Classify the preparation.
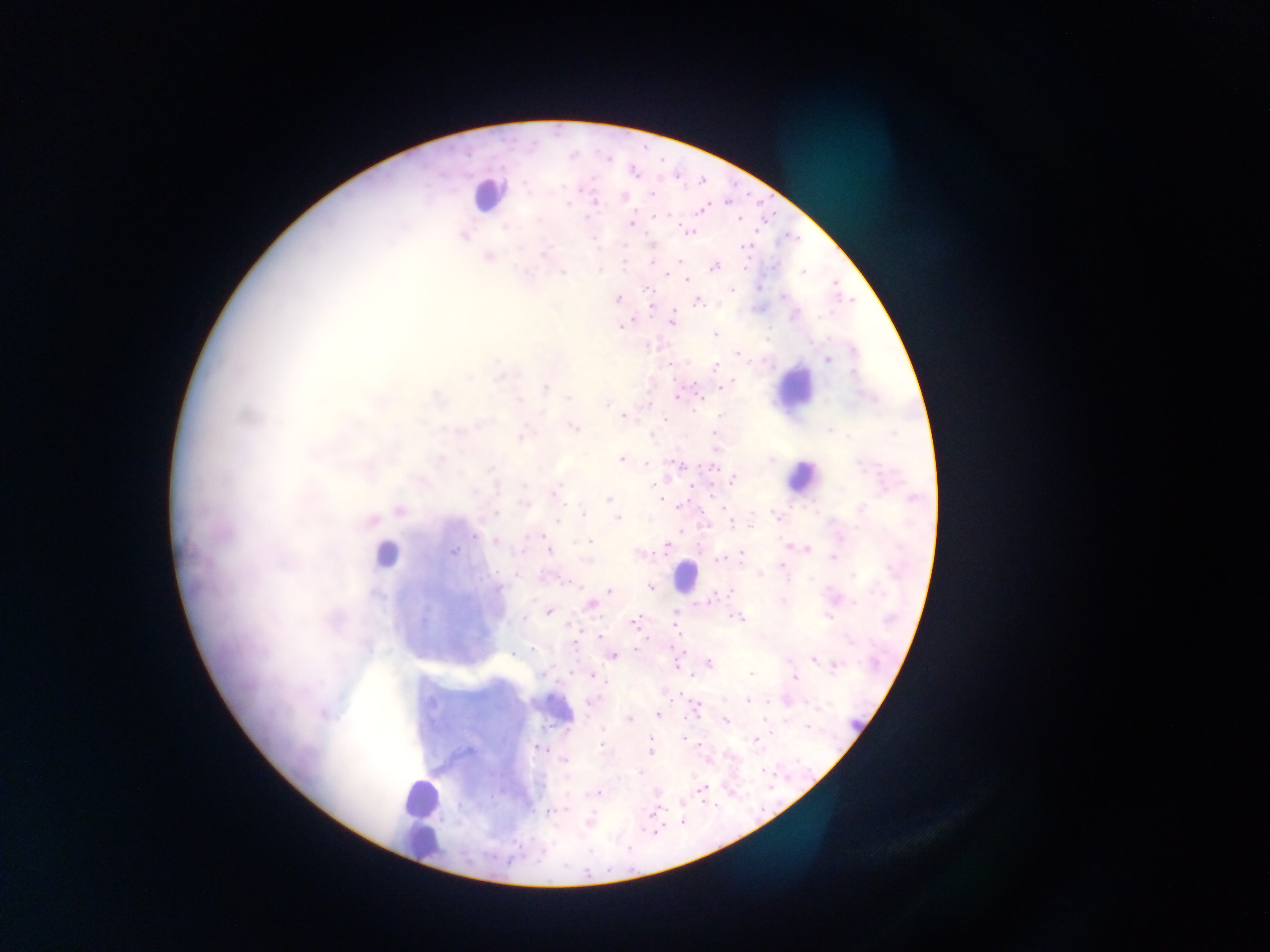

Thick blood film.

field of view = single
malaria parasite locations = approximate centers as [x, y] in pixels: [633, 172], [650, 195], [624, 196], [726, 203], [567, 204], [702, 209], [654, 218], [740, 220], [631, 224], [686, 234], [653, 245], [650, 248], [745, 249], [653, 261], [678, 261], [713, 267], [801, 273], [665, 276], [687, 281], [735, 290], [782, 296], [617, 297], [698, 302], [672, 320], [622, 326], [715, 334], [737, 355], [829, 360], [670, 364], [716, 366], [852, 371], [735, 380], [721, 387], [676, 397], [568, 398], [698, 399], [606, 403], [623, 415], [663, 418], [575, 428], [831, 431], [621, 458], [674, 461], [646, 463], [713, 466], [733, 479], [521, 485], [884, 489], [552, 494], [607, 497], [913, 498], [660, 499], [683, 503], [523, 504], [862, 508], [581, 512], [496, 513], [775, 516], [618, 519], [558, 523], [730, 524], [751, 525], [474, 536], [541, 536], [495, 541], [590, 542], [666, 544], [788, 546], [807, 548], [454, 551], [548, 552], [741, 554], [833, 558], [721, 559], [586, 560], [783, 567], [759, 575], [650, 586], [498, 587], [608, 591], [730, 591], [782, 599], [707, 602], [588, 604], [548, 612], [830, 618], [676, 619], [740, 619], [632, 622], [677, 627], [598, 636], [851, 641], [533, 648], [516, 654], [613, 656], [814, 661], [707, 663], [677, 665], [836, 666], [592, 674], [750, 674], [796, 679], [664, 691], [748, 701], [770, 701], [698, 708], [657, 715], [630, 719], [725, 722], [804, 727], [684, 739], [649, 742], [755, 742], [602, 746], [539, 748], [649, 752], [565, 759], [639, 774], [702, 790], [498, 791], [598, 793], [655, 793], [657, 808], [553, 811], [588, 820]
country = Ghana
image size = 1270×952 pixels
leukocyte locations = approximate centers as [x, y] in pixels: [486, 199], [383, 557], [417, 799], [422, 844]
capture = mobile-phone photograph through a microscope